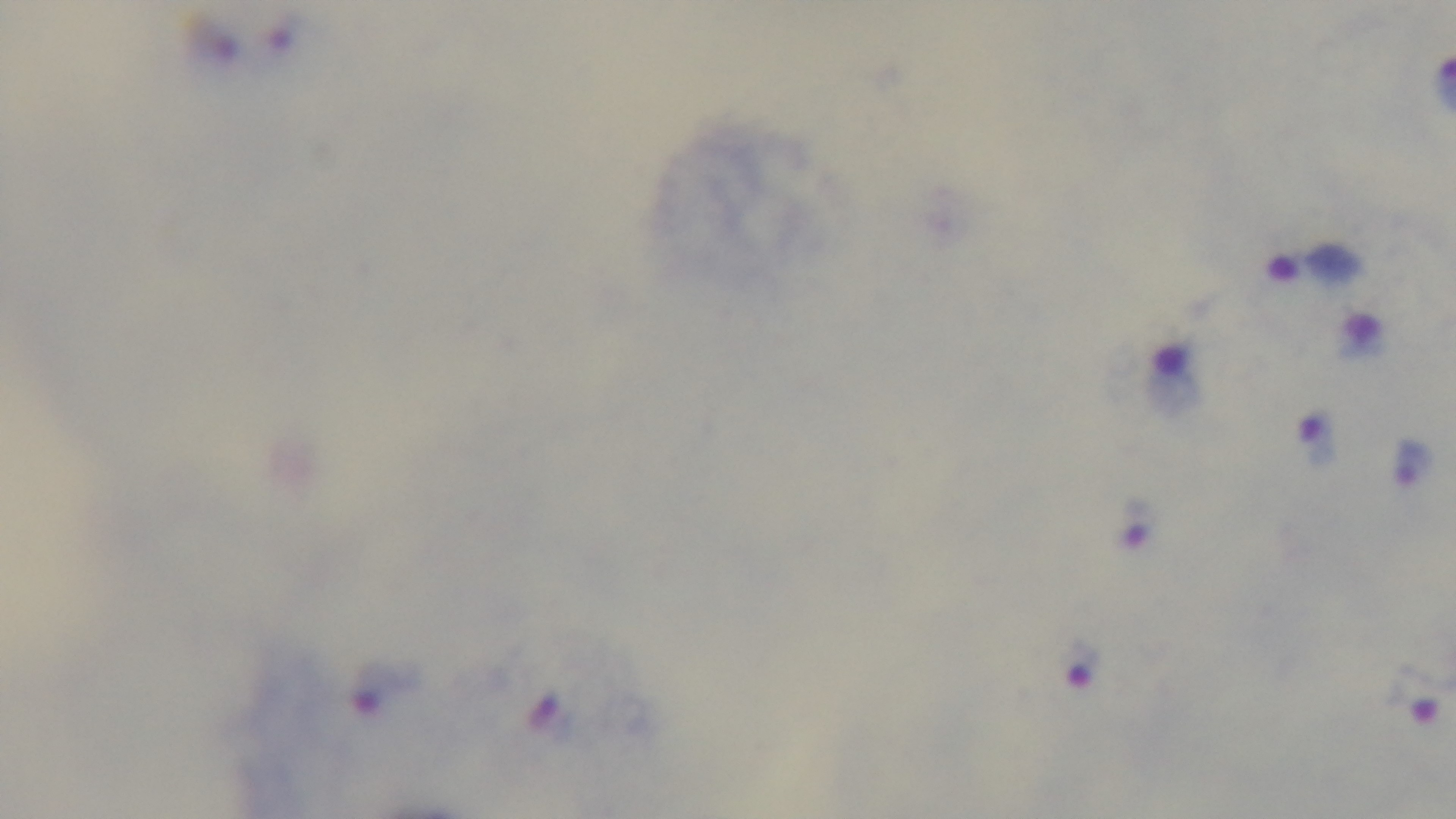
{
  "capture": "mounted 4K digital camera",
  "preparation": "thick",
  "objective": "100x oil immersion",
  "modality": "light microscopy",
  "field_of_view": "single",
  "stain": "Giemsa",
  "malaria_status": "positive"
}